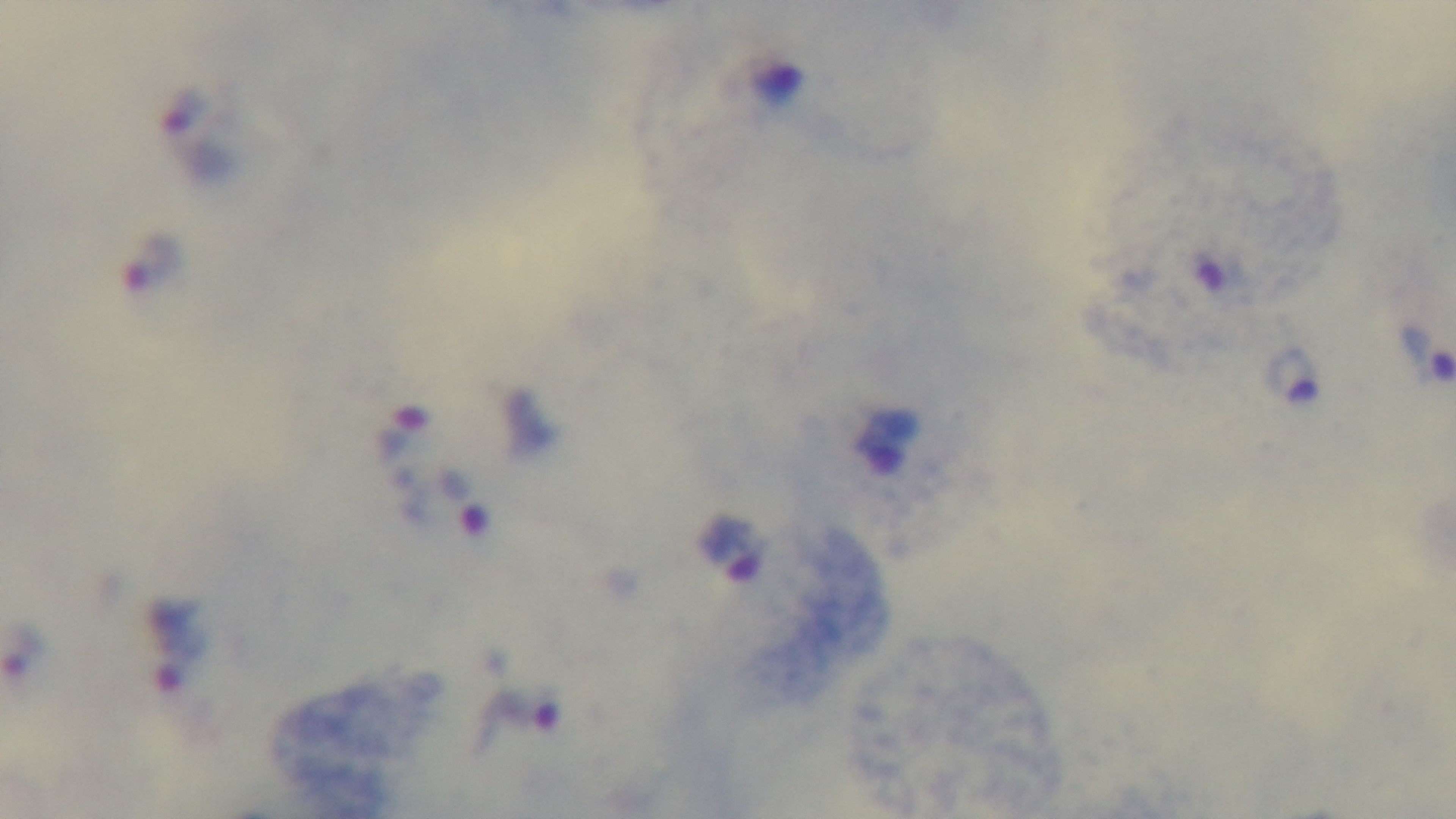

field of view = one from the slide
malaria status = positive
objective = 100x oil immersion
stain = Giemsa
modality = light microscopy
capture = mounted 4K digital camera
preparation = thick blood film